Report the malaria status of this cell.
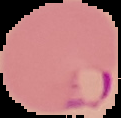
It is parasitized.

Cell region segmented out of the field of view; the surrounding area is masked to black. From a thin blood film. Image is 121×118 pixels.